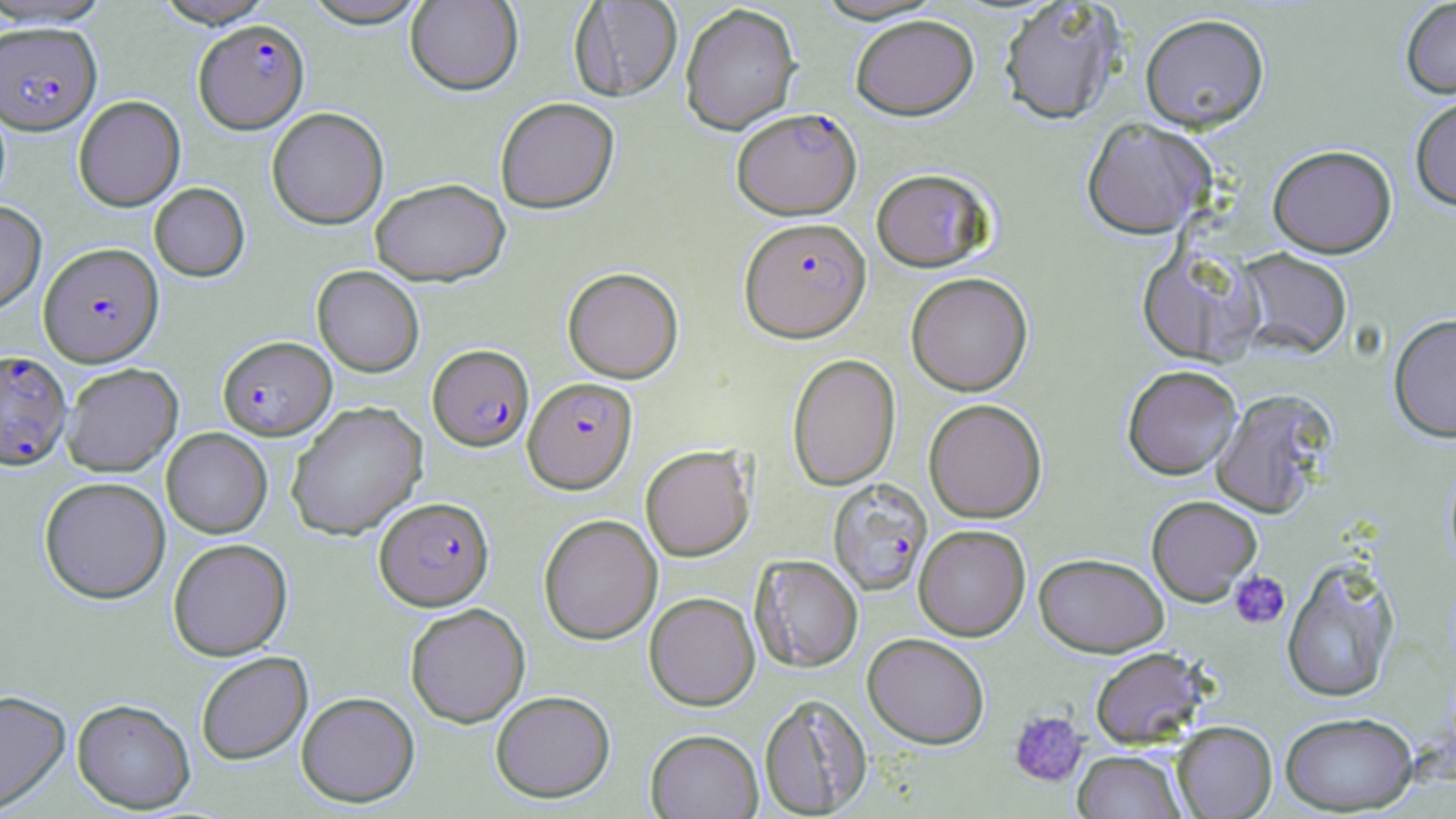 Approximate bounding boxes as named x1/y1/x2/y2 corners in pixels. Plasmodium falciparum-infected red blood cell locations: (x1=193, y1=19, x2=309, y2=133), (x1=0, y1=22, x2=101, y2=134), (x1=732, y1=107, x2=862, y2=219), (x1=740, y1=216, x2=872, y2=342), (x1=39, y1=242, x2=163, y2=366), (x1=217, y1=336, x2=336, y2=440), (x1=428, y1=343, x2=534, y2=451), (x1=0, y1=349, x2=71, y2=469), (x1=523, y1=377, x2=637, y2=493), (x1=827, y1=478, x2=932, y2=595), (x1=374, y1=496, x2=494, y2=610). Platelet locations: (x1=1229, y1=570, x2=1289, y2=629), (x1=1008, y1=709, x2=1087, y2=787). Uninfected red blood cell locations: (x1=0, y1=0, x2=114, y2=27), (x1=152, y1=0, x2=277, y2=28), (x1=299, y1=0, x2=432, y2=28), (x1=405, y1=0, x2=523, y2=96), (x1=810, y1=0, x2=948, y2=23), (x1=998, y1=0, x2=1126, y2=124), (x1=1400, y1=0, x2=1456, y2=98), (x1=569, y1=1, x2=683, y2=101), (x1=679, y1=3, x2=801, y2=135), (x1=1140, y1=13, x2=1269, y2=132), (x1=850, y1=14, x2=979, y2=120), (x1=1410, y1=94, x2=1456, y2=210), (x1=73, y1=95, x2=185, y2=212), (x1=495, y1=97, x2=620, y2=214), (x1=266, y1=107, x2=388, y2=229), (x1=1080, y1=118, x2=1215, y2=239), (x1=1268, y1=144, x2=1397, y2=257), (x1=871, y1=167, x2=994, y2=272), (x1=370, y1=178, x2=511, y2=286), (x1=149, y1=183, x2=250, y2=281), (x1=0, y1=201, x2=47, y2=314), (x1=1136, y1=245, x2=1261, y2=366), (x1=1234, y1=248, x2=1353, y2=359), (x1=312, y1=265, x2=424, y2=377), (x1=562, y1=267, x2=683, y2=383), (x1=906, y1=272, x2=1032, y2=396), (x1=1388, y1=313, x2=1456, y2=442), (x1=787, y1=353, x2=901, y2=491), (x1=61, y1=363, x2=183, y2=476), (x1=1122, y1=365, x2=1242, y2=480), (x1=1211, y1=388, x2=1336, y2=518), (x1=923, y1=398, x2=1047, y2=523), (x1=286, y1=401, x2=427, y2=540), (x1=162, y1=428, x2=272, y2=538), (x1=640, y1=445, x2=755, y2=561), (x1=39, y1=476, x2=171, y2=604), (x1=1146, y1=495, x2=1263, y2=605), (x1=538, y1=513, x2=662, y2=644), (x1=914, y1=524, x2=1031, y2=640), (x1=168, y1=538, x2=292, y2=660), (x1=1034, y1=552, x2=1169, y2=656), (x1=750, y1=555, x2=863, y2=672), (x1=1281, y1=558, x2=1400, y2=703), (x1=644, y1=592, x2=760, y2=710), (x1=405, y1=603, x2=530, y2=727), (x1=862, y1=632, x2=990, y2=748), (x1=1089, y1=647, x2=1212, y2=749), (x1=196, y1=651, x2=312, y2=764), (x1=0, y1=690, x2=70, y2=814), (x1=491, y1=690, x2=615, y2=803), (x1=296, y1=691, x2=420, y2=807), (x1=758, y1=693, x2=872, y2=817), (x1=72, y1=698, x2=195, y2=813), (x1=1280, y1=711, x2=1418, y2=815), (x1=1171, y1=721, x2=1276, y2=818), (x1=645, y1=729, x2=763, y2=818), (x1=1073, y1=750, x2=1187, y2=818). Slide-level diagnosis: Plasmodium falciparum. Captured at 1000x magnification. May-Grünwald-Giemsa stain. Single field of view. Light microscopy. Image is 1456×819 pixels. Thin blood smear.